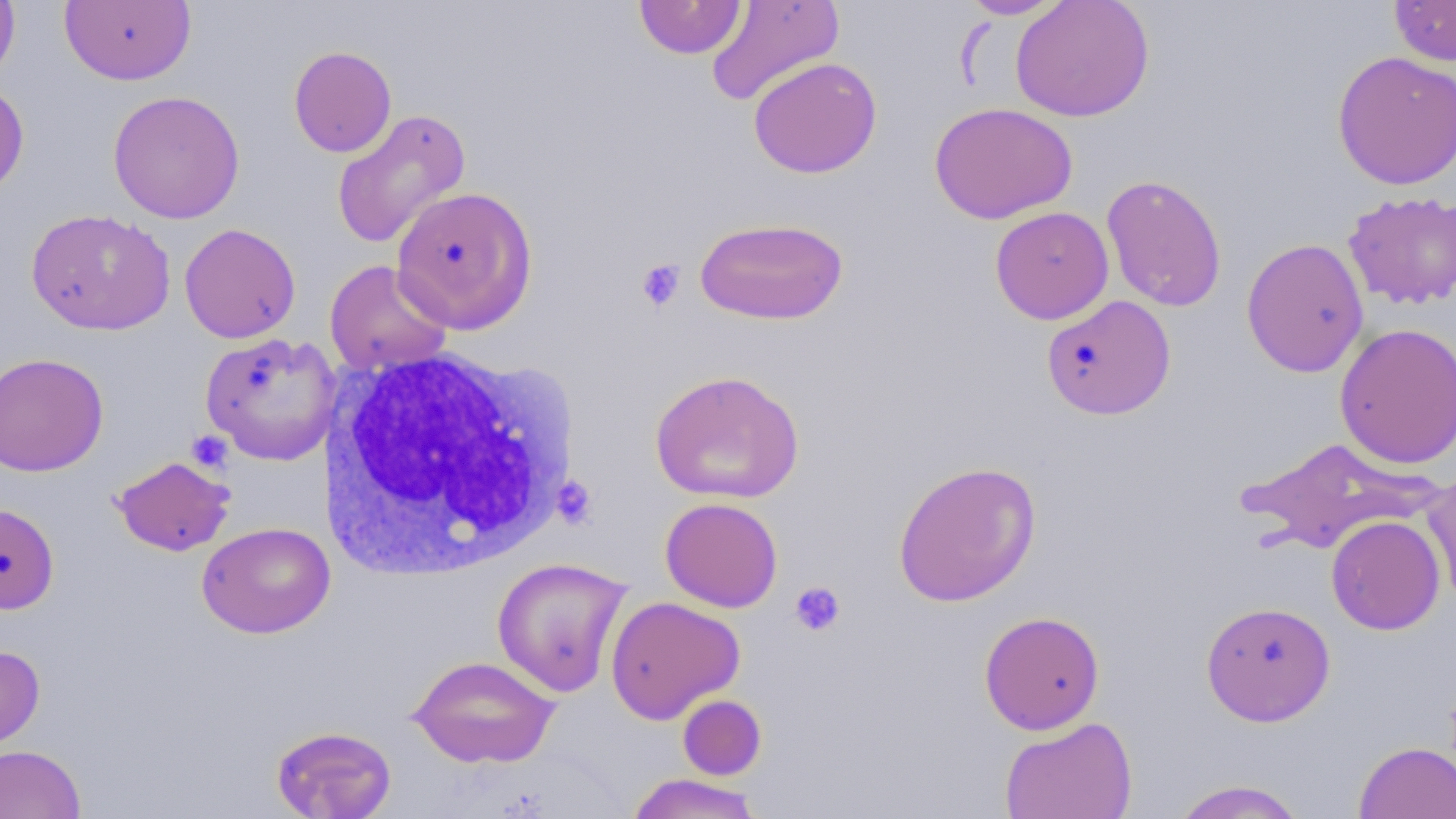

{
  "slide_level_diagnosis": "no evidence of blood parasites",
  "stain": "May-Grünwald-Giemsa",
  "white_blood_cell_locations": "approximate bounding boxes as named x1/y1/x2/y2 corners in pixels: (x1=318, y1=345, x2=575, y2=580)",
  "uninfected_red_blood_cell_locations": "approximate bounding boxes as named x1/y1/x2/y2 corners in pixels: (x1=0, y1=0, x2=20, y2=84), (x1=60, y1=0, x2=196, y2=86), (x1=633, y1=0, x2=747, y2=59), (x1=705, y1=0, x2=845, y2=107), (x1=958, y1=0, x2=1069, y2=20), (x1=1009, y1=0, x2=1154, y2=122), (x1=1389, y1=0, x2=1456, y2=66), (x1=288, y1=46, x2=397, y2=158), (x1=1332, y1=51, x2=1456, y2=190), (x1=748, y1=56, x2=883, y2=179), (x1=0, y1=79, x2=29, y2=199), (x1=107, y1=90, x2=246, y2=223), (x1=929, y1=102, x2=1078, y2=225), (x1=330, y1=108, x2=471, y2=249), (x1=1101, y1=174, x2=1228, y2=312), (x1=390, y1=185, x2=538, y2=333), (x1=1342, y1=190, x2=1456, y2=310), (x1=989, y1=206, x2=1114, y2=324), (x1=24, y1=209, x2=176, y2=336), (x1=694, y1=216, x2=849, y2=325), (x1=179, y1=223, x2=301, y2=344), (x1=1241, y1=237, x2=1370, y2=377), (x1=324, y1=259, x2=454, y2=376), (x1=1041, y1=295, x2=1176, y2=420), (x1=1334, y1=322, x2=1456, y2=469), (x1=199, y1=332, x2=339, y2=464), (x1=0, y1=352, x2=108, y2=477), (x1=649, y1=369, x2=805, y2=504), (x1=1236, y1=436, x2=1441, y2=553), (x1=112, y1=456, x2=236, y2=556), (x1=892, y1=460, x2=1042, y2=608), (x1=1421, y1=467, x2=1456, y2=606), (x1=660, y1=497, x2=783, y2=613), (x1=0, y1=502, x2=59, y2=615), (x1=1326, y1=515, x2=1445, y2=635), (x1=197, y1=521, x2=335, y2=639), (x1=492, y1=556, x2=632, y2=697), (x1=605, y1=595, x2=745, y2=724), (x1=1201, y1=600, x2=1336, y2=726), (x1=979, y1=610, x2=1105, y2=734), (x1=0, y1=644, x2=45, y2=751), (x1=407, y1=654, x2=560, y2=769), (x1=677, y1=694, x2=767, y2=780), (x1=999, y1=715, x2=1138, y2=819), (x1=270, y1=725, x2=397, y2=819), (x1=1354, y1=741, x2=1456, y2=819), (x1=0, y1=744, x2=85, y2=819), (x1=625, y1=773, x2=765, y2=818), (x1=1170, y1=779, x2=1310, y2=819)",
  "preparation": "thin blood smear",
  "field_of_view": "single",
  "magnification": "1000x",
  "image_size": "1456×819 pixels",
  "modality": "light microscopy",
  "platelet_locations": "approximate bounding boxes as named x1/y1/x2/y2 corners in pixels: (x1=635, y1=258, x2=686, y2=312), (x1=186, y1=431, x2=233, y2=472), (x1=552, y1=476, x2=597, y2=529), (x1=789, y1=581, x2=846, y2=637)"
}